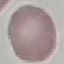

Malaria status: uninfected. Cell patch, automatically extracted from a larger field of view and resized to 64 × 64 pixels. Giemsa-stained preparation. Acquired by smartphone through the microscope eyepiece. Thin smear of blood.